Locate Plasmodium parasites and leukocytes.
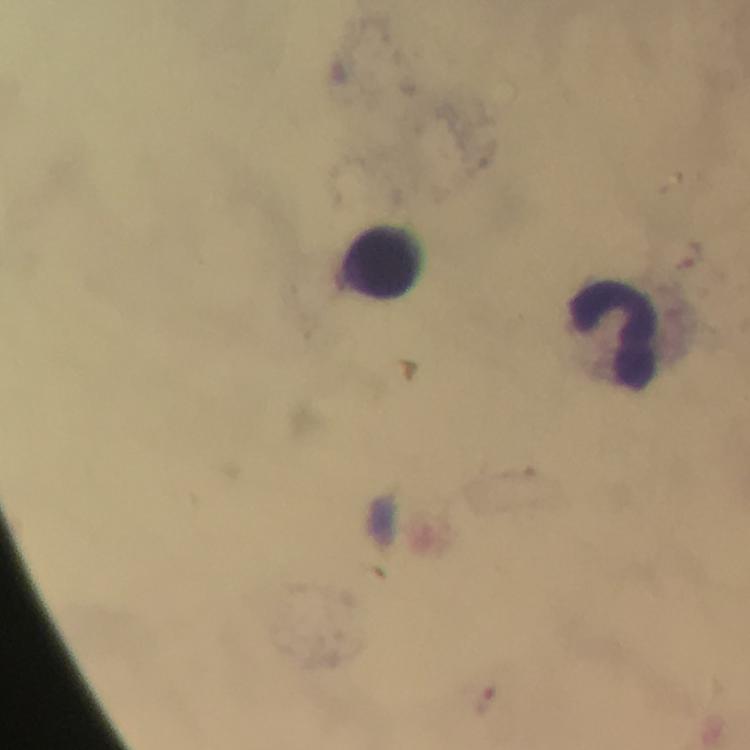
Approximate centers as [x, y] in pixels.
Plasmodium parasites: [693, 254], [485, 705].
Leukocytes: [383, 262], [612, 336].

{
  "stain": "Giemsa",
  "image_size": "750×750 pixels",
  "immersion_oil": "used",
  "context": "from a diagnostic examination for malaria",
  "capture": "smartphone camera through the microscope",
  "cropped_from": "a single field of view",
  "preparation": "thick blood film",
  "magnification": "100x"
}